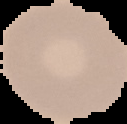
Summary:
  - Preparation: thin blood film
  - Image size: 127×124 pixels
  - Malaria status: uninfected
  - Image type: cell region segmented out of the field of view; surrounding area masked to black